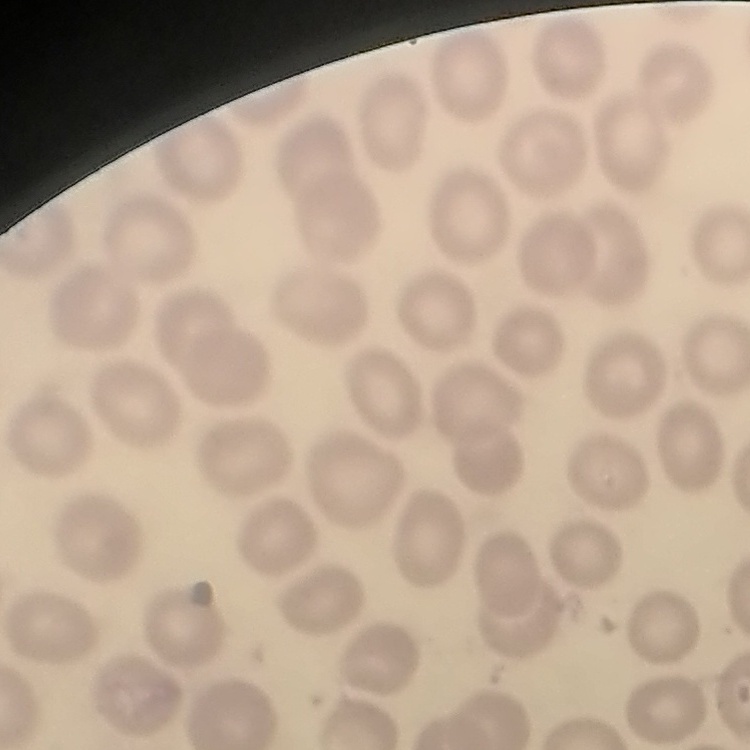

Summary:
  - Red blood cell morphology: no rouleaux formation
  - Stain: Field's or Giemsa
  - Image type: square crop of a larger photomicrograph
  - Preparation: thin blood smear